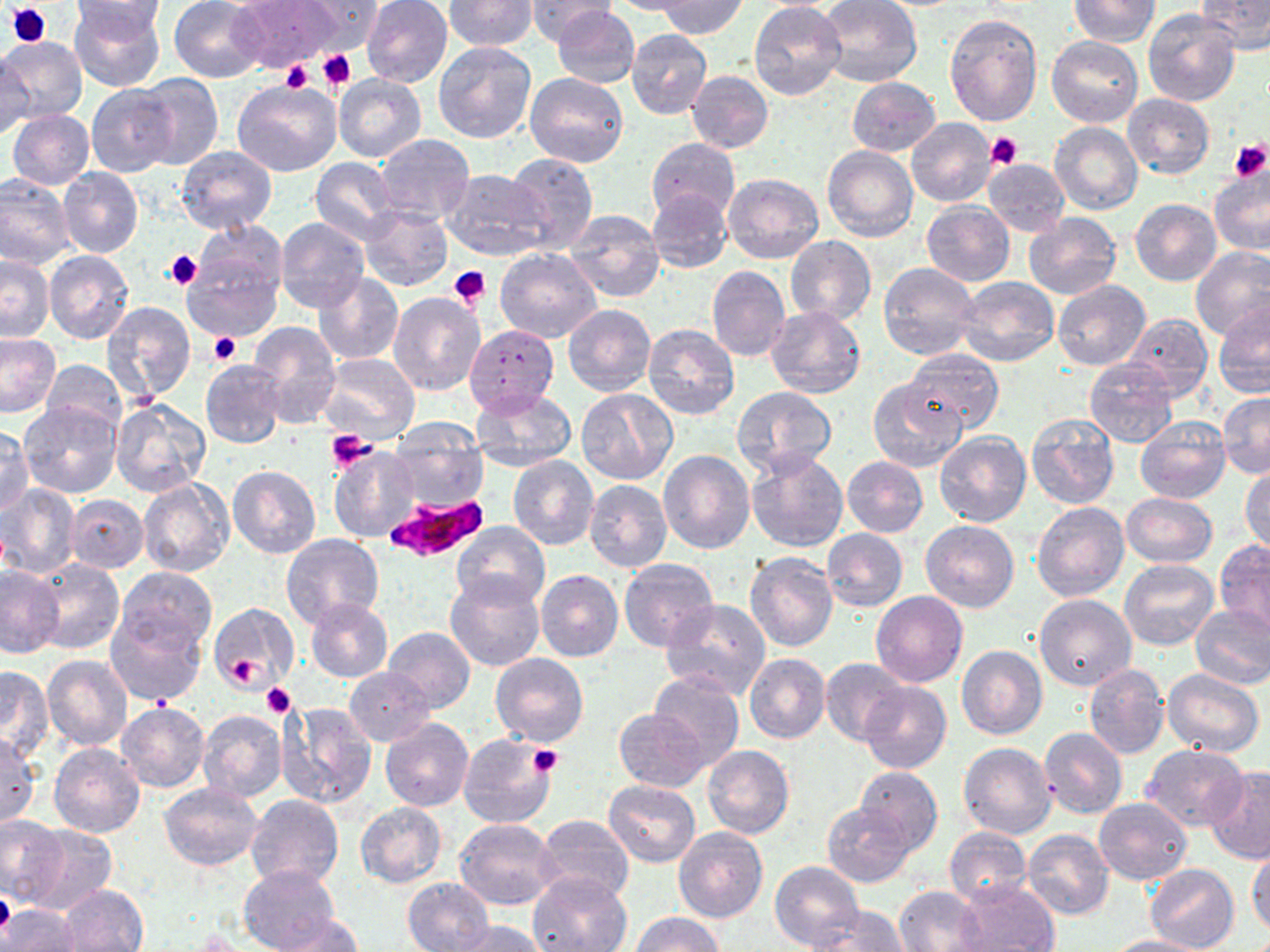
Approximate bounding boxes as (x1,y1)-(x2,y2) corner pairs in pixels. Plasmodium falciparum-infected red blood cell locations: (384,495)-(489,564). Uninfected red blood cell locations: (169,0)-(268,82), (229,0)-(341,73), (298,0)-(384,50), (524,0)-(617,45), (604,0)-(709,16), (816,0)-(922,88), (1194,0)-(1269,55), (70,1)-(164,92), (361,1)-(452,87), (444,1)-(537,50), (656,1)-(749,39), (1069,1)-(1159,46), (71,2)-(169,34), (750,4)-(845,99), (553,5)-(640,88), (1143,8)-(1242,107), (944,14)-(1042,126), (626,29)-(712,119), (0,35)-(87,124), (1047,36)-(1143,127), (432,41)-(536,143), (0,55)-(31,143), (525,71)-(628,167), (687,71)-(773,152), (131,73)-(223,169), (333,73)-(427,162), (847,77)-(941,156), (234,78)-(341,176), (87,86)-(179,176), (1123,94)-(1214,178), (12,98)-(173,186), (8,110)-(94,190), (907,117)-(996,207), (1050,122)-(1143,216), (375,134)-(474,225), (647,138)-(740,221), (174,146)-(277,234), (822,146)-(918,243), (503,152)-(598,254), (311,158)-(402,244), (982,159)-(1070,236), (59,167)-(143,257), (441,169)-(550,261), (1208,169)-(1270,257), (945,172)-(1064,264), (722,173)-(823,263), (0,175)-(74,269), (646,189)-(733,272), (1131,199)-(1222,286), (922,202)-(1015,285), (360,205)-(452,289), (562,209)-(665,303), (1023,214)-(1122,300), (275,217)-(368,313), (190,221)-(288,305), (785,236)-(876,325), (1190,247)-(1270,340), (180,248)-(282,342), (495,248)-(601,343), (44,249)-(134,344), (0,255)-(54,341), (878,261)-(980,359), (707,266)-(790,362), (312,273)-(404,365), (956,276)-(1059,366), (1053,280)-(1149,371), (387,292)-(484,396), (1213,301)-(1270,399), (102,302)-(197,405), (564,305)-(656,396), (767,305)-(865,399), (1123,312)-(1213,400), (249,322)-(341,429), (643,323)-(739,420), (464,324)-(558,415), (0,333)-(61,418), (903,351)-(1005,434), (318,354)-(419,443), (1083,357)-(1180,447), (200,358)-(286,448), (40,359)-(125,437), (868,379)-(967,473), (732,386)-(836,476), (470,387)-(577,469), (576,387)-(678,485), (1217,392)-(1270,478), (110,398)-(211,498), (20,402)-(121,499), (1025,410)-(1120,509), (1135,415)-(1230,503), (385,420)-(490,513), (0,425)-(33,516), (934,430)-(1031,527), (328,447)-(420,541), (658,449)-(754,554), (745,450)-(849,552), (508,456)-(599,550), (841,456)-(928,538), (1241,465)-(1269,556), (228,466)-(320,559), (138,478)-(234,579), (584,480)-(672,573), (1,484)-(81,577), (1119,492)-(1217,567), (65,495)-(149,572), (1032,501)-(1129,602), (920,520)-(1020,613), (454,521)-(550,611), (821,529)-(908,612), (280,533)-(383,629), (1214,537)-(1270,638), (744,552)-(838,653), (28,559)-(123,655), (619,559)-(720,653), (1119,559)-(1219,651), (0,565)-(66,659), (117,567)-(216,656), (536,569)-(624,662), (445,572)-(546,672), (870,590)-(967,687), (1035,593)-(1136,691), (305,597)-(394,682), (662,599)-(770,699), (209,602)-(298,695), (1190,604)-(1270,689), (105,612)-(206,706), (383,627)-(475,712), (663,633)-(769,751), (956,645)-(1049,740), (490,653)-(589,747), (744,653)-(831,744), (43,656)-(133,751), (822,659)-(909,746), (1084,664)-(1168,759), (0,665)-(53,762), (345,667)-(435,746), (1162,668)-(1263,756), (647,671)-(743,771), (860,681)-(951,774), (117,700)-(209,793), (279,701)-(376,808), (614,708)-(709,791), (198,709)-(287,803), (380,719)-(473,810), (1039,727)-(1127,819), (458,733)-(558,829), (0,735)-(41,827), (958,741)-(1057,839), (50,743)-(145,838), (702,744)-(795,839), (1139,744)-(1249,831), (1203,765)-(1270,863), (854,766)-(942,856), (604,781)-(700,866), (158,782)-(263,869), (245,795)-(343,890), (1094,798)-(1191,884), (822,799)-(916,887), (355,802)-(447,888), (0,813)-(68,908), (535,815)-(635,902), (454,818)-(562,910), (23,825)-(115,915), (944,827)-(1032,908), (674,828)-(768,924), (1022,830)-(1114,920), (1247,845)-(1270,939), (770,862)-(864,951), (1145,864)-(1239,950), (239,865)-(341,952), (530,873)-(631,952), (402,876)-(495,952), (953,878)-(1058,952), (59,884)-(147,952), (896,886)-(986,951), (2,904)-(80,952), (809,905)-(909,951), (630,912)-(726,952), (277,914)-(362,952), (453,921)-(549,952), (1106,936)-(1208,952). Platelet locations: (6,2)-(50,49), (317,49)-(355,92), (282,61)-(314,95), (986,131)-(1023,169), (1230,137)-(1269,181), (164,248)-(203,288), (450,267)-(491,308), (210,330)-(240,364), (325,429)-(378,471), (225,654)-(260,688), (261,684)-(295,718), (530,744)-(562,777), (0,887)-(15,939). Slide-level diagnosis: Plasmodium falciparum. Thin blood smear. May-Grünwald-Giemsa stain. Image is 1270×952 pixels. Optical microscopy. 1000x magnification. Single field of view.